Name the cell type shown.
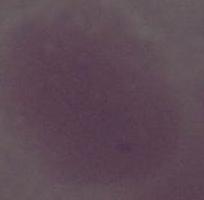
An erythrocyte.

magnification = 1000x
modality = photomicrograph